Report the malaria status of this cell.
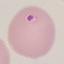
Parasitized.

Photographed with a smartphone camera at the microscope eyepiece. Giemsa-stained preparation. Cell patch, automatically extracted from a larger field of view and resized to 64 × 64 pixels. Thin blood film.